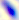 Photomicrograph. Toxoplasma gondii is seen. Captured at 400x magnification.